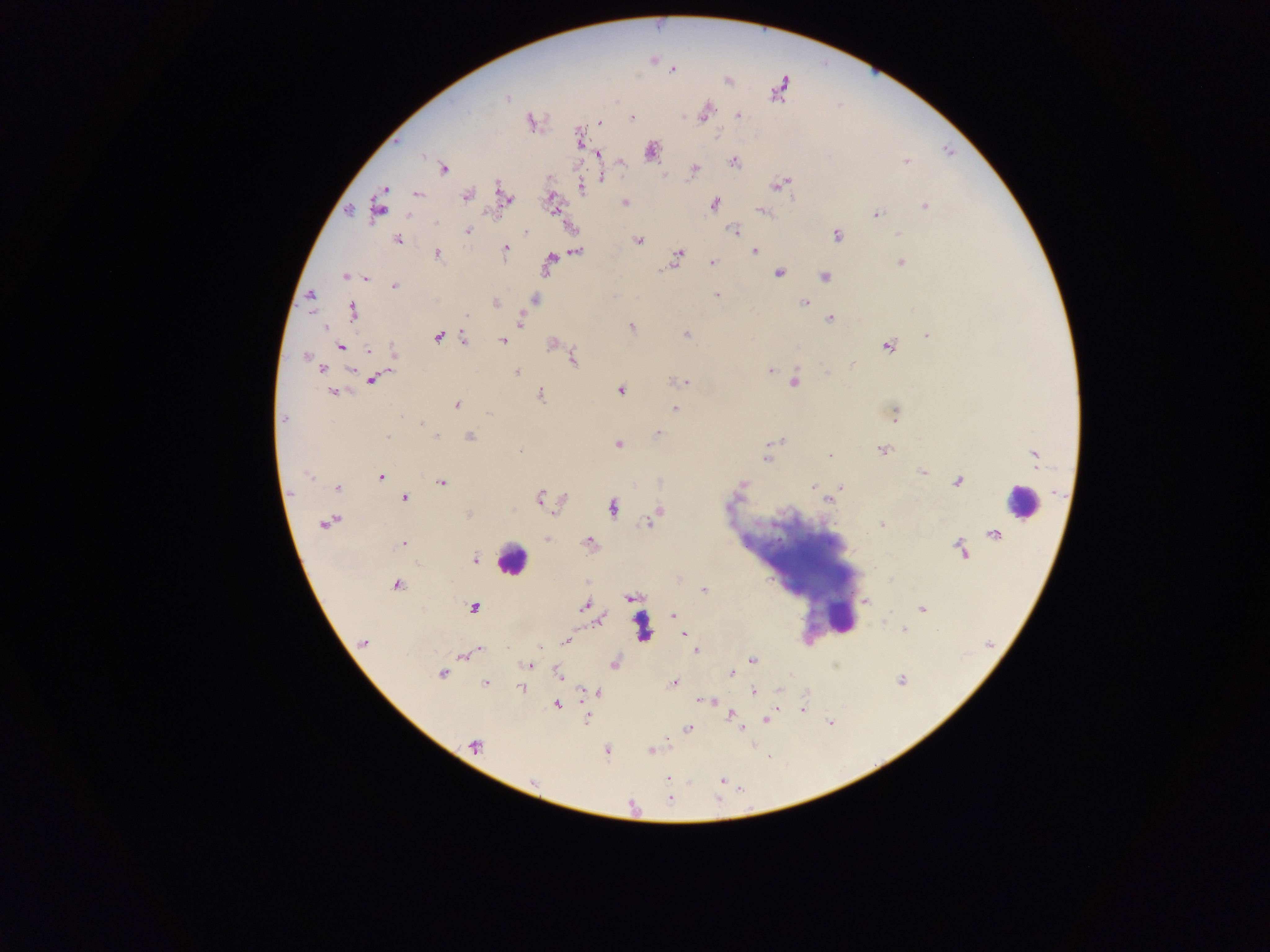 Approximate centers as x y in pixels. Plasmodium parasite locations: 671 72; 782 84; 507 98; 738 115; 702 117; 633 118; 529 121; 599 123; 718 133; 599 154; 735 162; 906 162; 443 168; 695 168; 601 178; 789 182; 777 185; 581 187; 419 195; 466 196; 512 199; 624 200; 715 204; 926 205; 762 210; 554 211; 495 213; 878 214; 434 222; 734 229; 467 231; 527 233; 897 233; 836 234; 398 240; 639 241; 506 247; 755 249; 577 250; 437 253; 677 253; 550 259; 711 261; 900 262; 779 274; 343 276; 825 276; 369 279; 394 284; 718 296; 804 303; 354 311; 465 315; 830 319; 521 320; 630 325; 326 329; 686 335; 926 336; 439 337; 464 337; 501 341; 553 345; 368 350; 392 355; 306 357; 573 357; 853 366; 322 369; 827 370; 517 371; 771 371; 685 382; 795 384; 621 391; 332 393; 542 393; 456 404; 675 407; 488 414; 892 415; 283 419; 422 424; 427 426; 658 433; 469 436; 387 437; 437 437; 780 439; 617 446; 520 450; 882 450; 830 455; 1034 455; 765 457; 921 471; 308 473; 381 477; 441 482; 742 485; 841 485; 338 486; 812 486; 840 488; 738 490; 289 492; 404 498; 539 498; 830 499; 562 500; 613 508; 660 510; 469 515; 332 521; 324 524; 881 526; 548 538; 588 541; 403 543; 476 559; 395 583; 585 583; 704 591; 628 597; 865 600; 584 607; 473 608; 923 610; 672 614; 604 615; 903 631; 685 632; 565 641; 365 642; 478 649; 695 651; 472 653; 462 657; 752 659; 613 664; 526 665; 730 673; 441 674; 558 676; 901 681; 485 683; 675 683; 520 689; 599 691; 751 694; 697 701; 558 705; 730 713; 768 720; 688 728; 740 728; 473 747; 649 751; 606 752; 669 778; 721 781; 669 800. Leukocyte locations: 1022 498; 508 560. Mobile-phone photograph taken through the microscope. One field of view. Collected in Ghana. Image is 1270×952 pixels. Thick blood film.